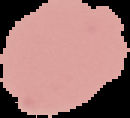

Summary:
  - Image type: segmented cell region on a black background
  - Result: negative for malaria parasites
  - Image size: 130×118 pixels
  - Preparation: thin blood film